State the preparation type.
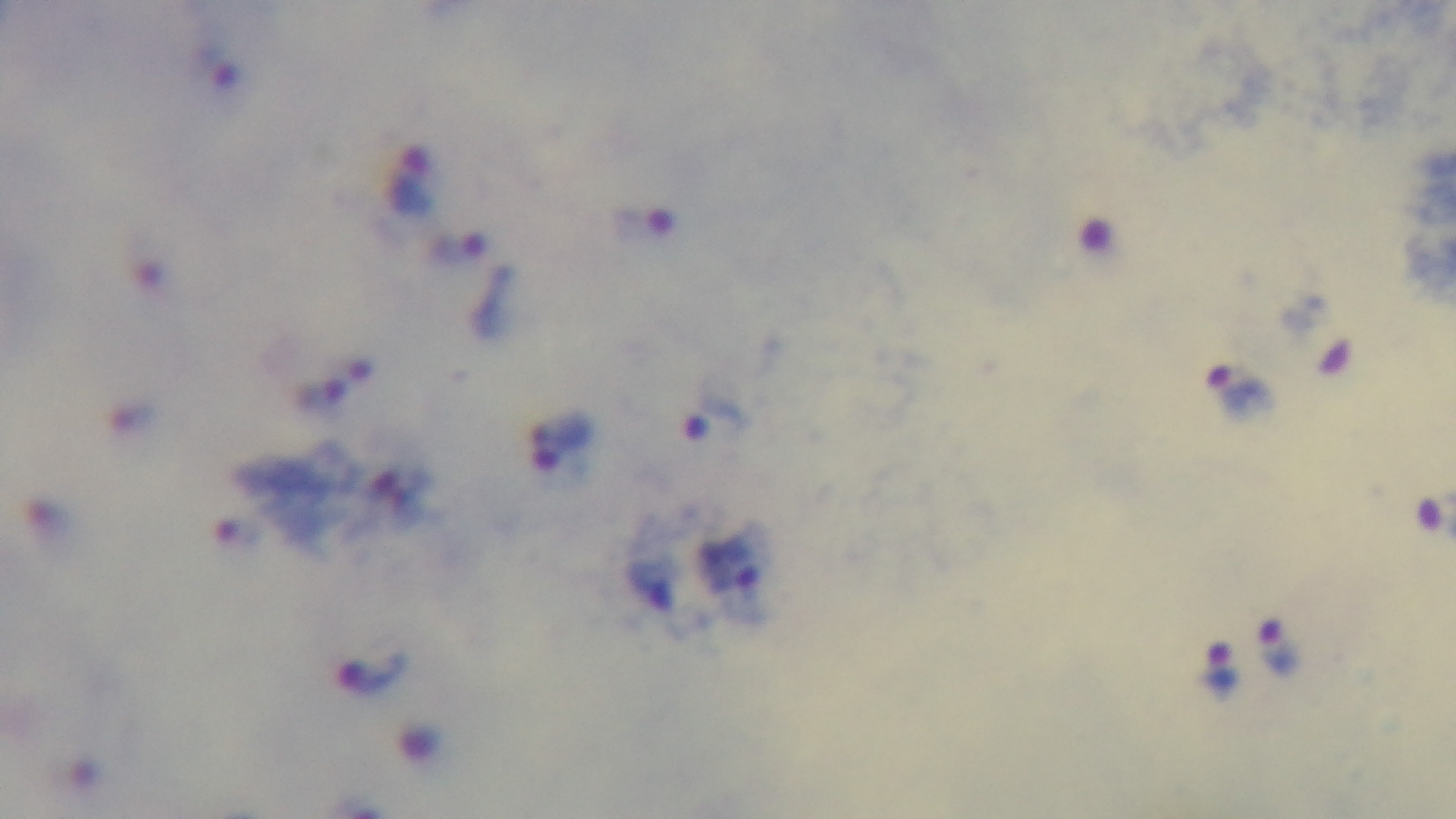
It is a thick blood film.

Giemsa-stained. One field from the slide. Oil-immersion objective, 100x. Mounted 4K digital camera. Light microscopy. Malaria status: positive.